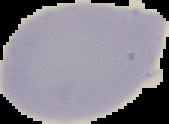 From a thin blood film. Segmented cell region on a black background. Image is 169×124 pixels. Malaria status: uninfected.